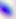

Toxoplasma gondii is shown. Photomicrograph. 400x magnification.